State which parasite is depicted.
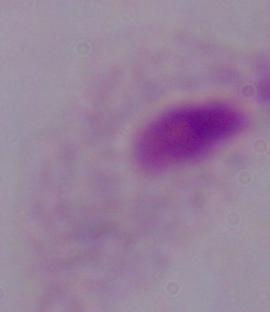
A trichomonad.

Summary:
  - Modality: photomicrograph
  - Magnification: 1000x